Comment on the morphology of the erythrocytes.
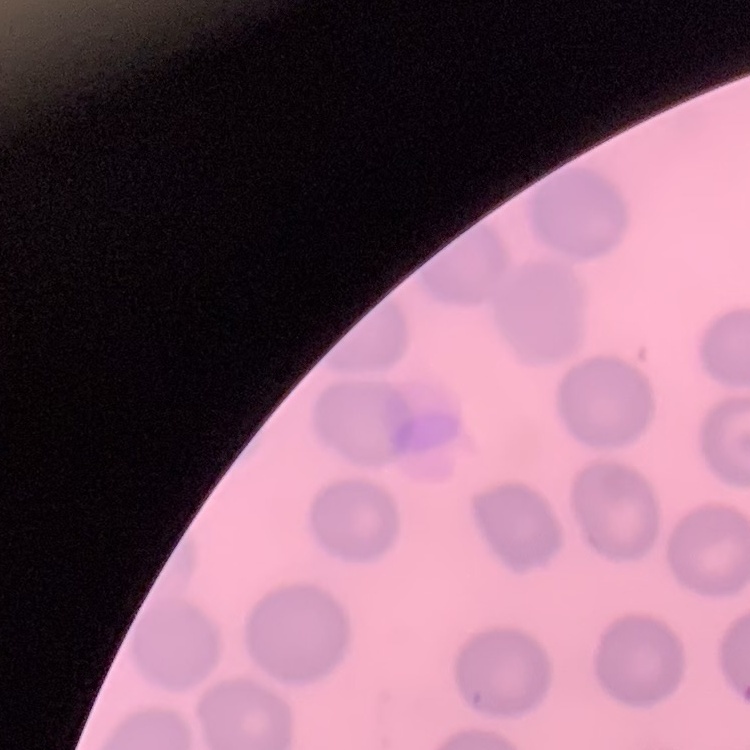
They show no rouleaux formation.

{
  "preparation": "thin blood film",
  "image_type": "one tile cut from a larger photomicrograph",
  "stain": "Field's or Giemsa"
}